Comment on the morphology of the red blood cells.
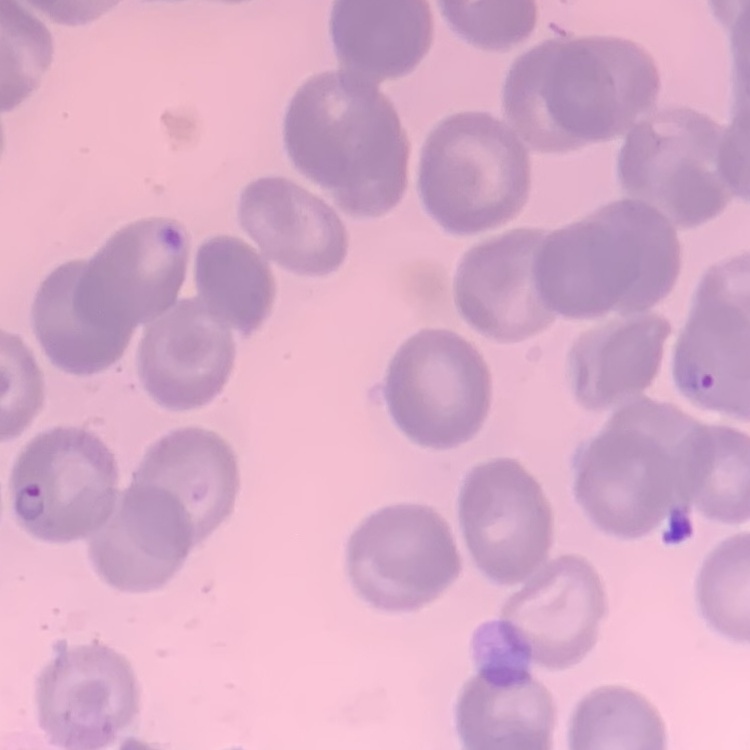

No rouleaux formation.

stain = Field's or Giemsa
image type = one tile cut from a larger photomicrograph
preparation = thin blood film